Locate every leukocyte (white blood cell).
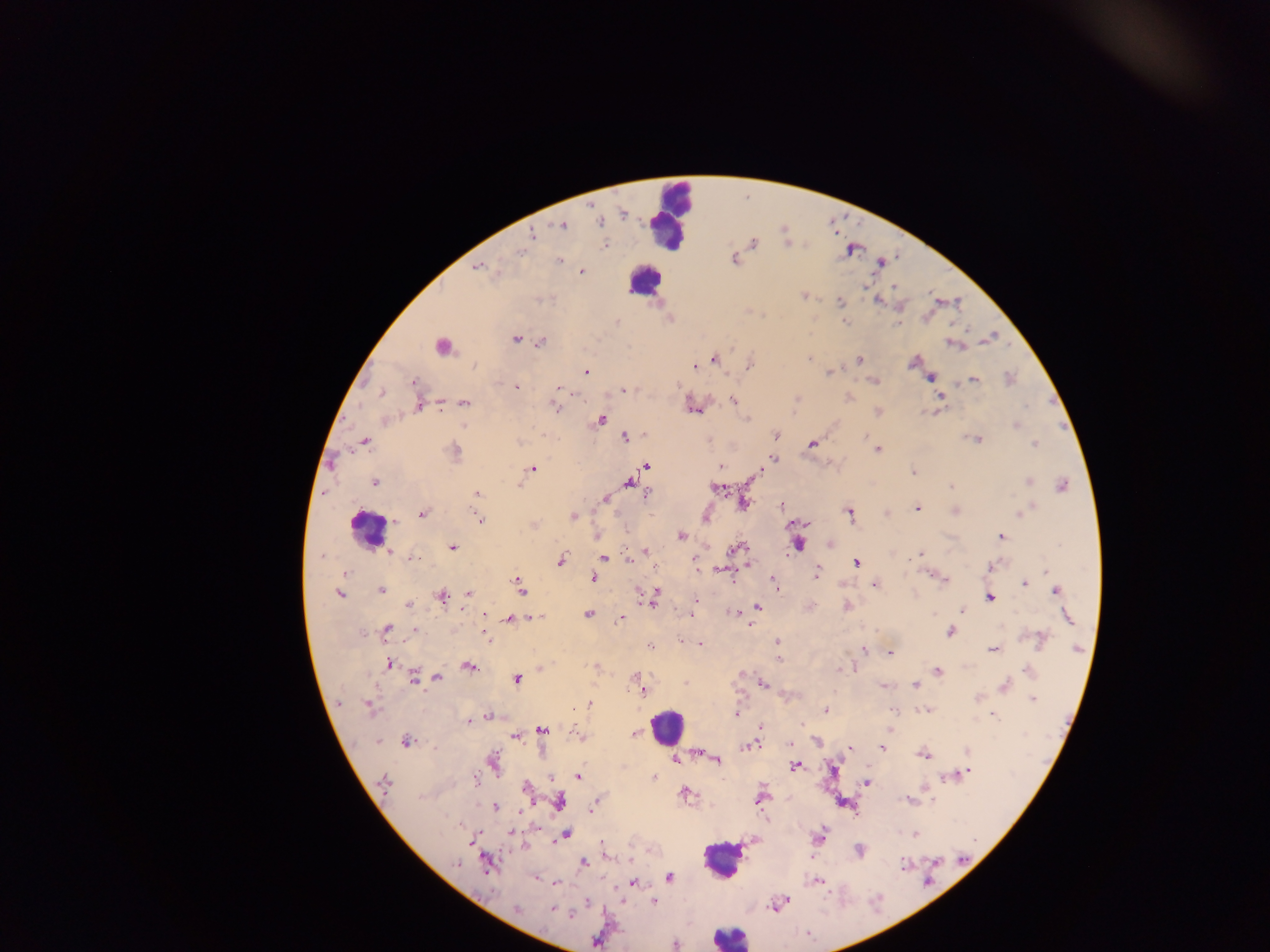
Approximate centers as x y in pixels.
Leukocytes: 670 218; 641 285; 369 529; 670 726; 720 860; 732 932.

preparation = thick blood film
country = Ghana
Plasmodium parasite locations = approximate centers as x y in pixels: 623 214; 599 222; 562 226; 532 234; 606 245; 517 253; 734 259; 560 260; 477 269; 581 270; 865 288; 895 288; 803 295; 879 299; 839 302; 960 303; 845 322; 968 328; 526 341; 542 342; 731 345; 810 358; 860 359; 713 360; 749 364; 693 367; 585 371; 828 372; 931 377; 973 378; 873 380; 413 382; 517 387; 556 387; 380 392; 622 392; 576 393; 940 397; 848 398; 440 401; 733 401; 465 404; 556 407; 418 408; 694 408; 440 409; 877 411; 748 418; 602 419; 462 425; 645 434; 775 436; 624 438; 364 440; 812 444; 453 445; 878 450; 774 459; 648 467; 532 468; 719 468; 913 470; 759 474; 374 482; 629 484; 1062 484; 950 485; 718 489; 477 495; 605 499; 746 502; 779 504; 917 508; 423 514; 850 514; 575 518; 480 519; 533 524; 681 535; 1002 536; 452 549; 645 550; 390 551; 921 553; 319 557; 562 558; 414 559; 606 559; 630 561; 855 562; 749 566; 719 569; 1045 570; 345 575; 818 575; 517 576; 592 578; 774 580; 946 581; 1023 582; 875 583; 382 591; 521 592; 1055 592; 470 593; 341 594; 650 596; 442 597; 989 598; 695 601; 409 605; 758 608; 846 608; 961 608; 587 614; 731 614; 485 615; 530 615; 934 615; 538 616; 690 616; 620 619; 510 621; 751 625; 388 628; 415 631; 949 632; 1040 636; 487 639; 776 641; 701 644; 1040 646; 650 647; 992 649; 862 650; 890 654; 779 659; 388 663; 596 666; 469 667; 853 669; 939 671; 636 676; 437 677; 415 678; 516 678; 686 682; 764 684; 883 686; 915 686; 644 693; 1033 700; 591 702; 336 704; 369 707; 827 709; 893 709; 575 710; 921 713; 996 716; 489 717; 470 722; 801 723; 759 727; 543 732; 635 733; 512 737; 405 741; 378 743; 753 745; 881 748; 850 750; 967 751; 923 756; 718 759; 676 760; 796 766; 970 770; 577 776; 654 776; 944 777; 549 779; 383 780; 475 783; 867 783; 525 788; 923 792; 686 794; 760 801; 906 802; 495 807; 590 810; 512 833; 567 835; 914 835; 601 841; 552 842; 611 856; 583 862; 455 865; 902 866; 484 867; 669 877; 816 877; 632 883; 789 899; 621 900; 654 902; 517 908; 551 909; 674 944
field of view = single
capture = mobile-phone photograph through a microscope
image size = 1270×952 pixels